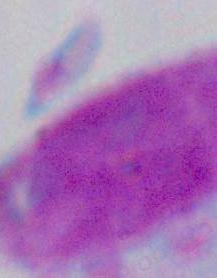

A white blood cell is seen. Photomicrograph. 1000x magnification.